Comment on the morphology of the red blood cells.
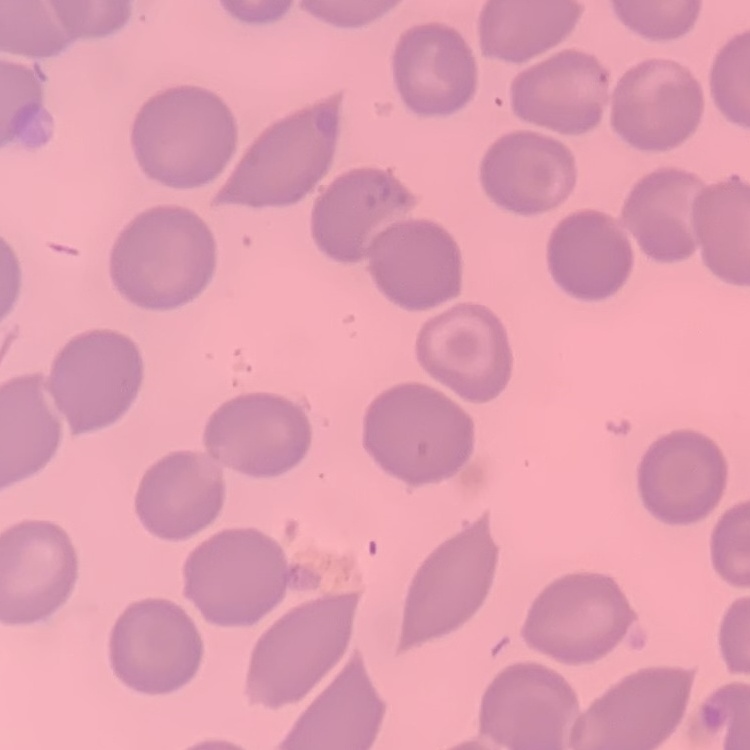
They show no rouleaux formation.

stain = Field's or Giemsa
image type = one tile cut from a larger photomicrograph
preparation = thin peripheral smear